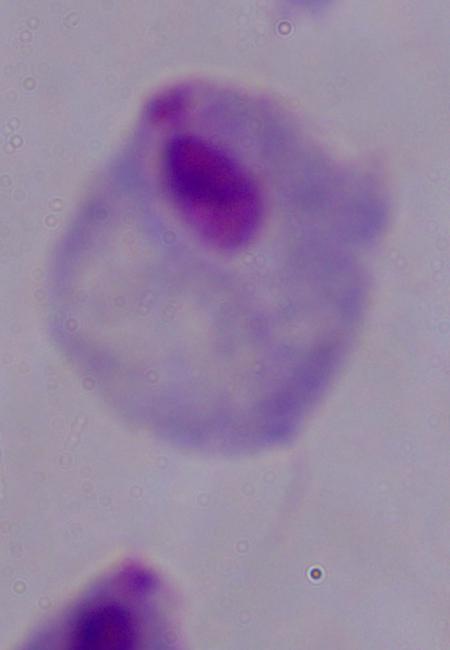
Summary:
  - Modality: micrograph
  - Identification: trichomonad
  - Magnification: 1000x